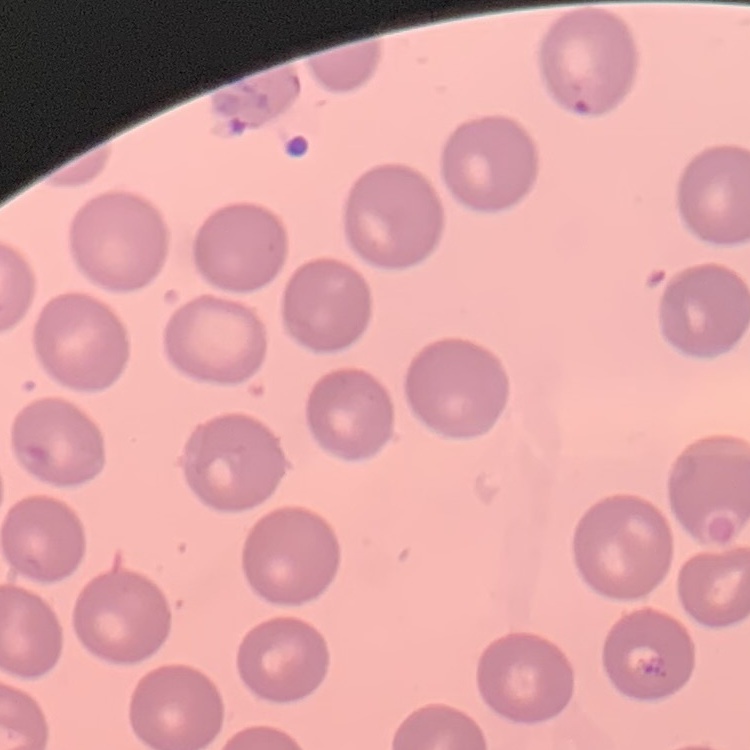
red blood cell morphology = no rouleaux formation
stain = Field's or Giemsa
preparation = thin peripheral smear
image type = one tile cut from a larger photomicrograph